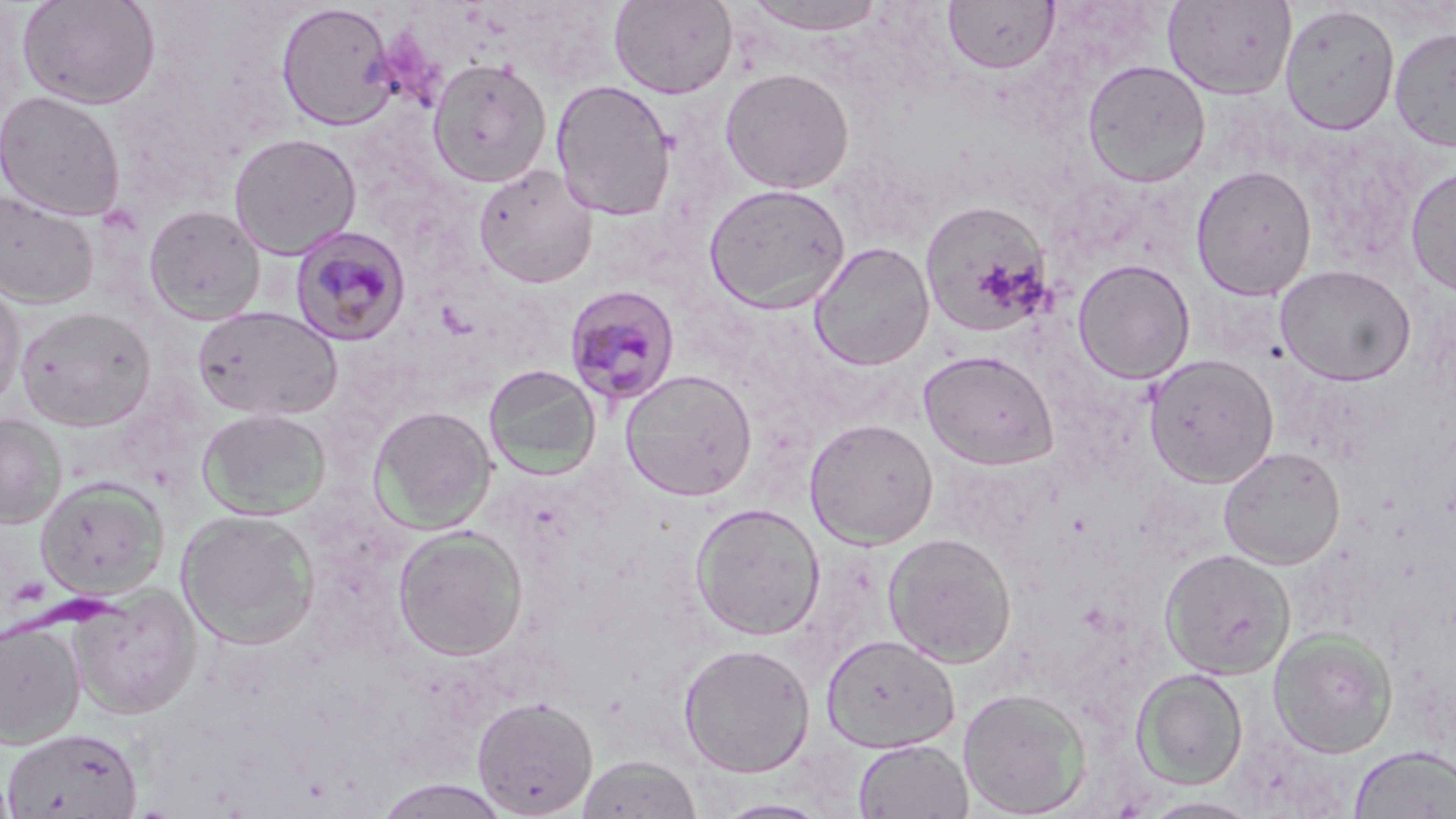
{
  "slide_level_diagnosis": "Plasmodium malariae",
  "preparation": "thin blood film",
  "platelet_locations": "approximate bounding boxes as (x1,y1)-(x2,y2) corner pairs in pixels: (8,575)-(50,607)",
  "field_of_view": "single",
  "image_size": "1456×819 pixels",
  "magnification": "1000x",
  "plasmodium_malariae_infected_red_blood_cell_locations": "approximate bounding boxes as (x1,y1)-(x2,y2) corner pairs in pixels: (290,224)-(412,346), (565,285)-(682,407)",
  "modality": "light microscopy",
  "stain": "May-Grünwald-Giemsa",
  "uninfected_red_blood_cell_locations": "approximate bounding boxes as (x1,y1)-(x2,y2) corner pairs in pixels: (17,0)-(160,109), (608,0)-(738,99), (743,0)-(890,35), (1163,0)-(1297,100), (943,1)-(1060,75), (276,2)-(398,131), (1279,4)-(1400,135), (1389,26)-(1456,152), (426,57)-(552,188), (1081,59)-(1211,187), (719,67)-(854,193), (550,79)-(677,221), (0,89)-(125,221), (228,132)-(362,259), (473,164)-(598,288), (1190,164)-(1317,300), (1405,165)-(1456,295), (703,183)-(851,313), (1,188)-(100,309), (920,201)-(1053,338), (143,204)-(266,325), (809,241)-(935,371), (1071,259)-(1196,384), (1275,264)-(1416,386), (0,278)-(25,411), (193,305)-(342,421), (16,306)-(155,431), (918,349)-(1058,470), (1143,353)-(1279,488), (482,363)-(601,480), (620,369)-(757,501), (369,405)-(497,533), (196,408)-(331,520), (0,414)-(66,529), (803,418)-(939,549), (1218,445)-(1345,569), (35,477)-(168,600), (690,502)-(825,640), (177,510)-(320,650), (392,526)-(528,661), (882,531)-(1017,667), (1159,548)-(1296,680), (69,584)-(202,719), (0,619)-(86,749), (1268,628)-(1398,758), (820,633)-(960,753), (678,642)-(815,778), (1132,668)-(1248,789), (958,687)-(1092,818), (471,696)-(598,818), (2,728)-(143,817), (852,738)-(973,819), (1349,746)-(1456,818), (576,754)-(703,819), (0,770)-(18,818), (372,779)-(512,818), (1139,796)-(1263,819), (713,798)-(835,818)"
}